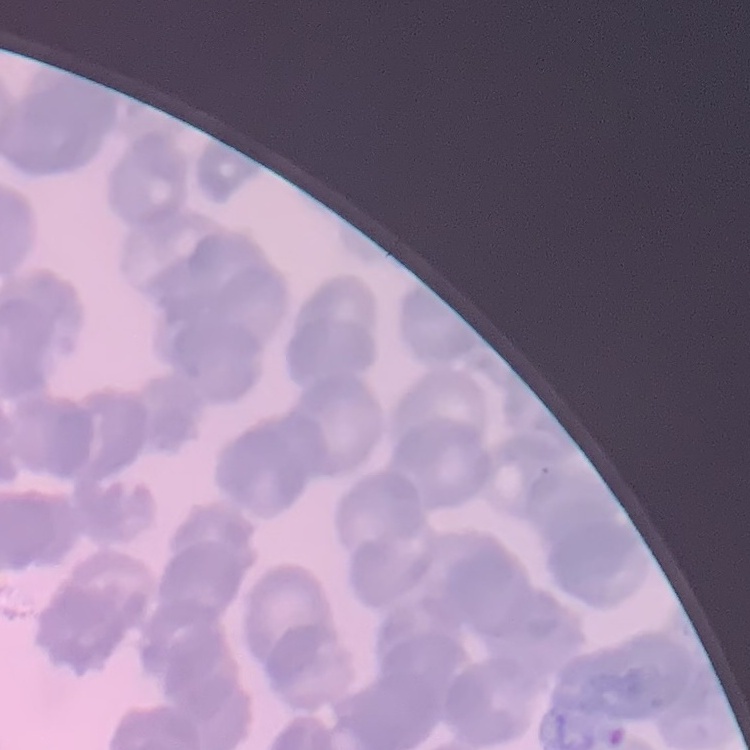
red blood cell morphology = rouleaux formation
preparation = thin peripheral smear
stain = Field's or Giemsa
image type = square crop of a larger photomicrograph